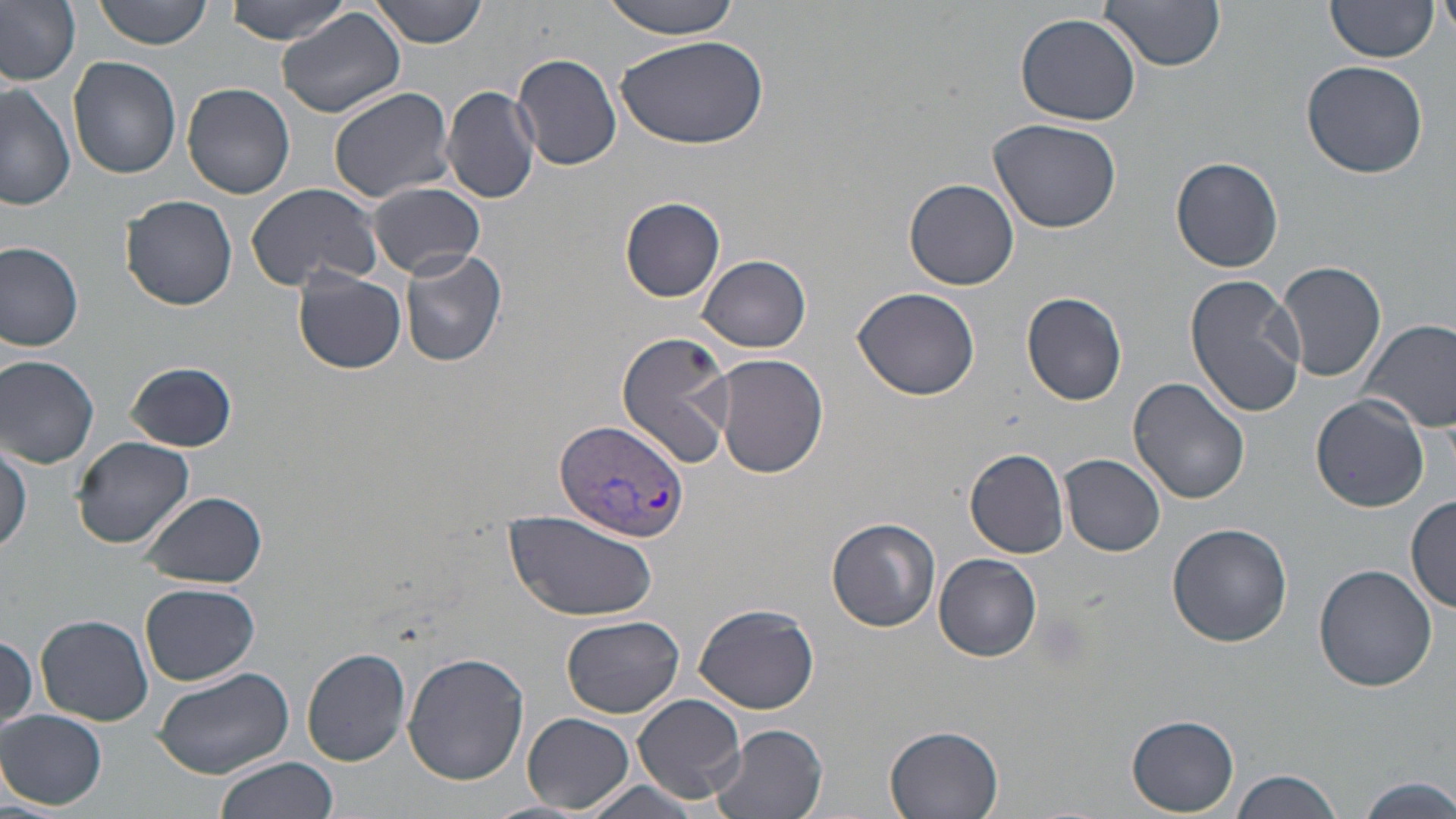

Summary:
  - Coordinate format: approximate bounding boxes as [x1, y1, x2, y2] in pixels
  - Plasmodium vivax-infected red blood cell locations: [554, 419, 688, 542]
  - Uninfected red blood cell locations: [93, 0, 216, 48], [223, 0, 352, 43], [373, 0, 489, 47], [601, 0, 742, 38], [1099, 0, 1224, 73], [1325, 0, 1437, 64], [1439, 0, 1456, 46], [0, 1, 81, 87], [277, 7, 405, 119], [1016, 11, 1143, 126], [616, 34, 769, 151], [511, 54, 625, 171], [69, 57, 181, 179], [1303, 61, 1428, 178], [0, 81, 76, 210], [182, 82, 296, 199], [329, 85, 455, 203], [441, 87, 542, 205], [989, 119, 1123, 234], [1171, 156, 1283, 273], [903, 178, 1020, 290], [367, 182, 486, 278], [245, 183, 385, 291], [121, 194, 237, 312], [620, 197, 725, 301], [0, 241, 84, 350], [400, 250, 507, 367], [699, 255, 811, 351], [1277, 260, 1387, 383], [293, 270, 407, 374], [1183, 275, 1307, 416], [851, 288, 983, 402], [1021, 292, 1130, 406], [1357, 316, 1456, 435], [615, 331, 733, 469], [1, 354, 100, 468], [712, 354, 829, 479], [124, 362, 237, 452], [1129, 377, 1251, 504], [1312, 394, 1429, 512], [73, 435, 195, 548], [0, 441, 32, 556], [966, 449, 1069, 558], [1061, 454, 1166, 557], [141, 490, 267, 588], [1407, 494, 1456, 614], [505, 516, 660, 622], [827, 517, 941, 631], [1167, 522, 1293, 647], [934, 553, 1042, 660], [1313, 563, 1437, 691], [141, 582, 260, 685], [695, 603, 821, 714], [36, 614, 153, 725], [560, 614, 685, 720], [0, 634, 37, 736], [301, 647, 412, 766], [402, 652, 529, 785], [154, 666, 295, 782], [631, 692, 747, 804], [1, 710, 106, 809], [523, 712, 633, 814], [1127, 715, 1240, 815], [708, 725, 828, 819], [885, 726, 1005, 819], [215, 757, 337, 819], [1232, 767, 1342, 819], [1354, 776, 1456, 817], [574, 777, 708, 819]
  - Slide-level diagnosis: Plasmodium vivax
  - Stain: May-Grünwald-Giemsa
  - Magnification: 1000x
  - Preparation: thin blood film
  - Field of view: single
  - Modality: light microscopy
  - Image size: 1456×819 pixels